Name the cell type shown.
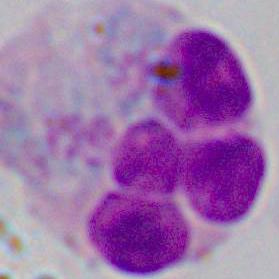

This is a leukocyte.

1000x magnification. Photomicrograph.